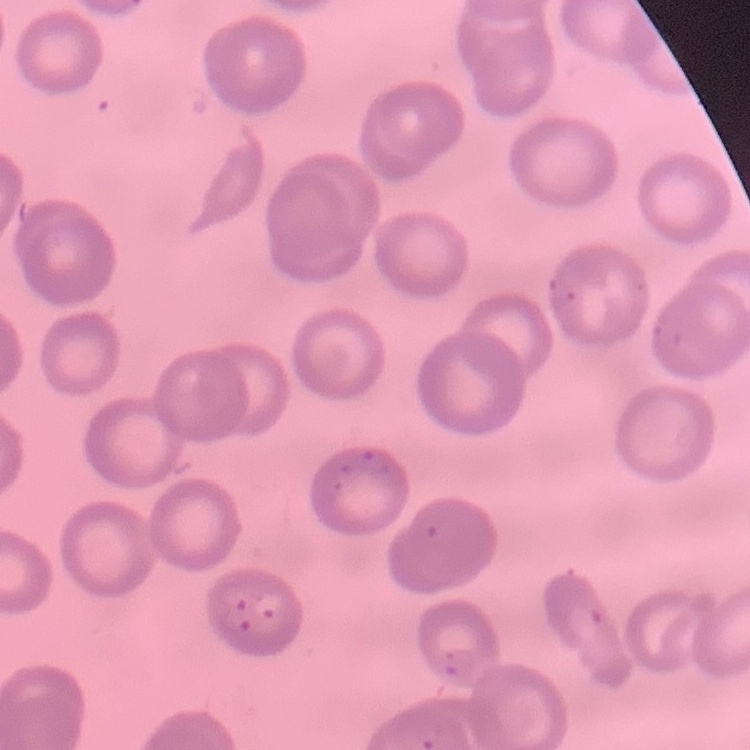
Summary:
  - Red blood cell morphology: no rouleaux formation
  - Stain: Field's or Giemsa
  - Preparation: thin blood smear
  - Image type: square crop of a larger photomicrograph